Classify this cell by malaria status.
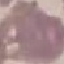
Uninfected.

Thin smear of blood. Automatically extracted cell patch, resized to 64 × 64 pixels. Photographed with a smartphone camera at the microscope eyepiece. Giemsa-stained preparation.